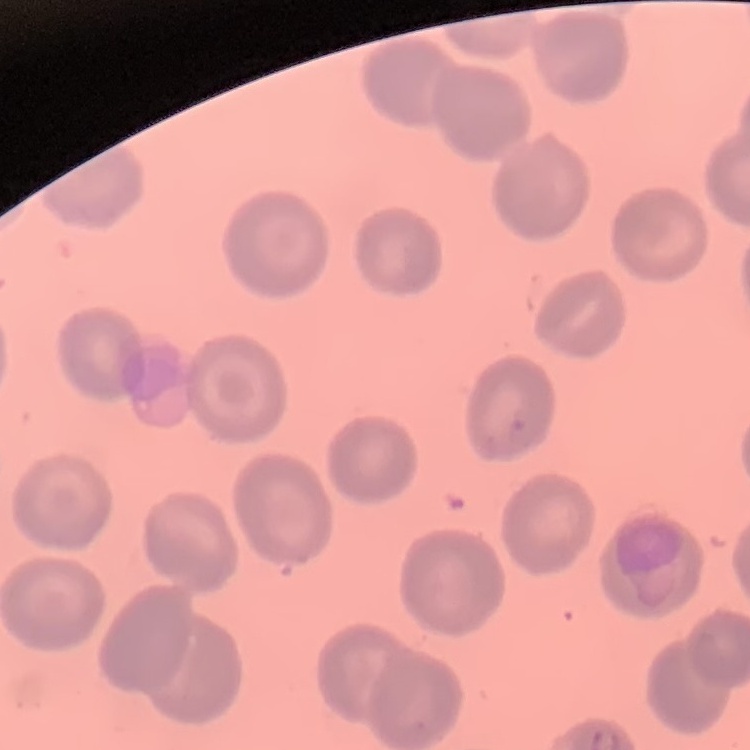
The erythrocytes show no rouleaux formation. Field's or Giemsa stain. Thin blood film. One tile cut from a larger photomicrograph.